Name the parasite shown.
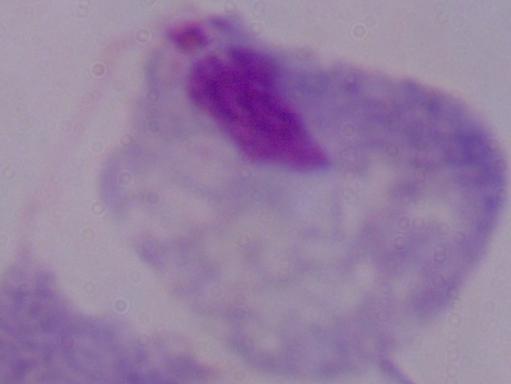
This is a trichomonad.

{
  "modality": "photomicrograph",
  "magnification": "1000x"
}